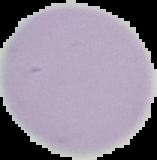
Summary:
  - Image size: 157×160 pixels
  - Preparation: thin blood film
  - Malaria status: uninfected
  - Image type: segmented cell region with the area outside set to black